Identify the parasite.
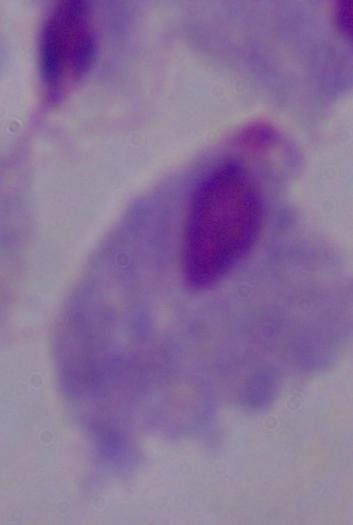
This is a trichomonad.

magnification = 1000x
modality = photomicrograph